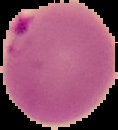
From a thin blood film. Result: Plasmodium parasites detected. Image is 118×130 pixels. Segmented cell region on a black background.